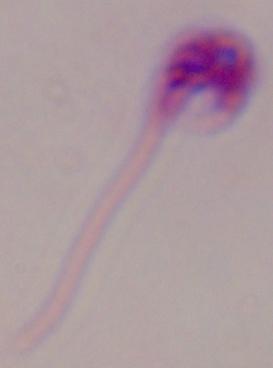
Micrograph. 1000x magnification. A Leishmania parasite is shown.